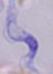
Summary:
  - Modality: photomicrograph
  - Magnification: 1000x
  - Identification: trypanosome